Point out each Plasmodium parasite.
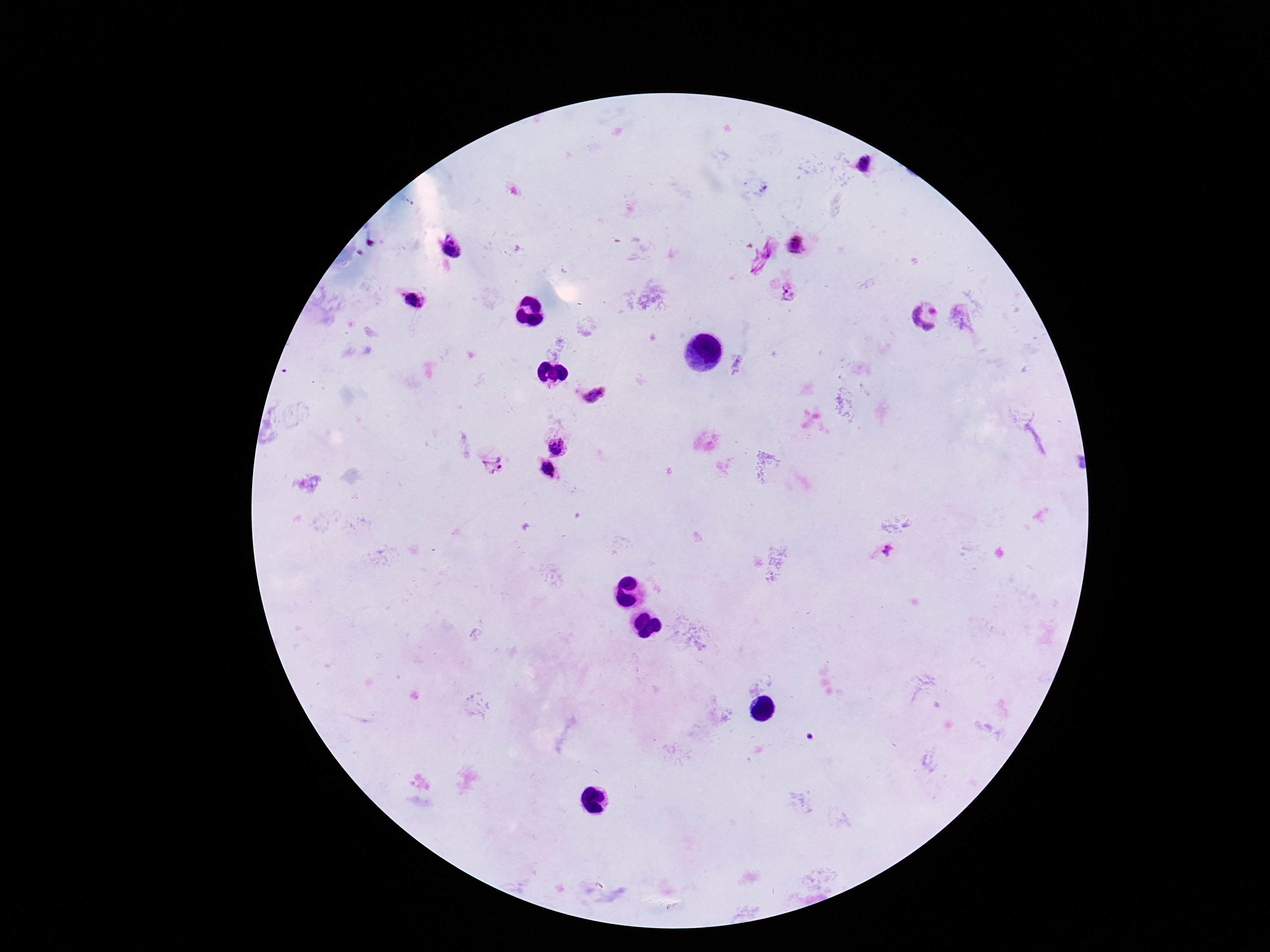
Approximate centers as [x, y] in pixels.
Plasmodium parasites: [863, 164], [797, 244], [453, 246], [768, 249], [758, 267], [790, 292], [413, 297], [927, 315], [593, 394], [558, 446], [491, 464], [546, 468], [887, 549].

Patient malaria status: positive. Thick peripheral-blood smear. 100x magnification. Giemsa stain. Image is 1270×952 pixels. One field from this slide. Smartphone photograph taken through the microscope eyepiece.